Find each WBC.
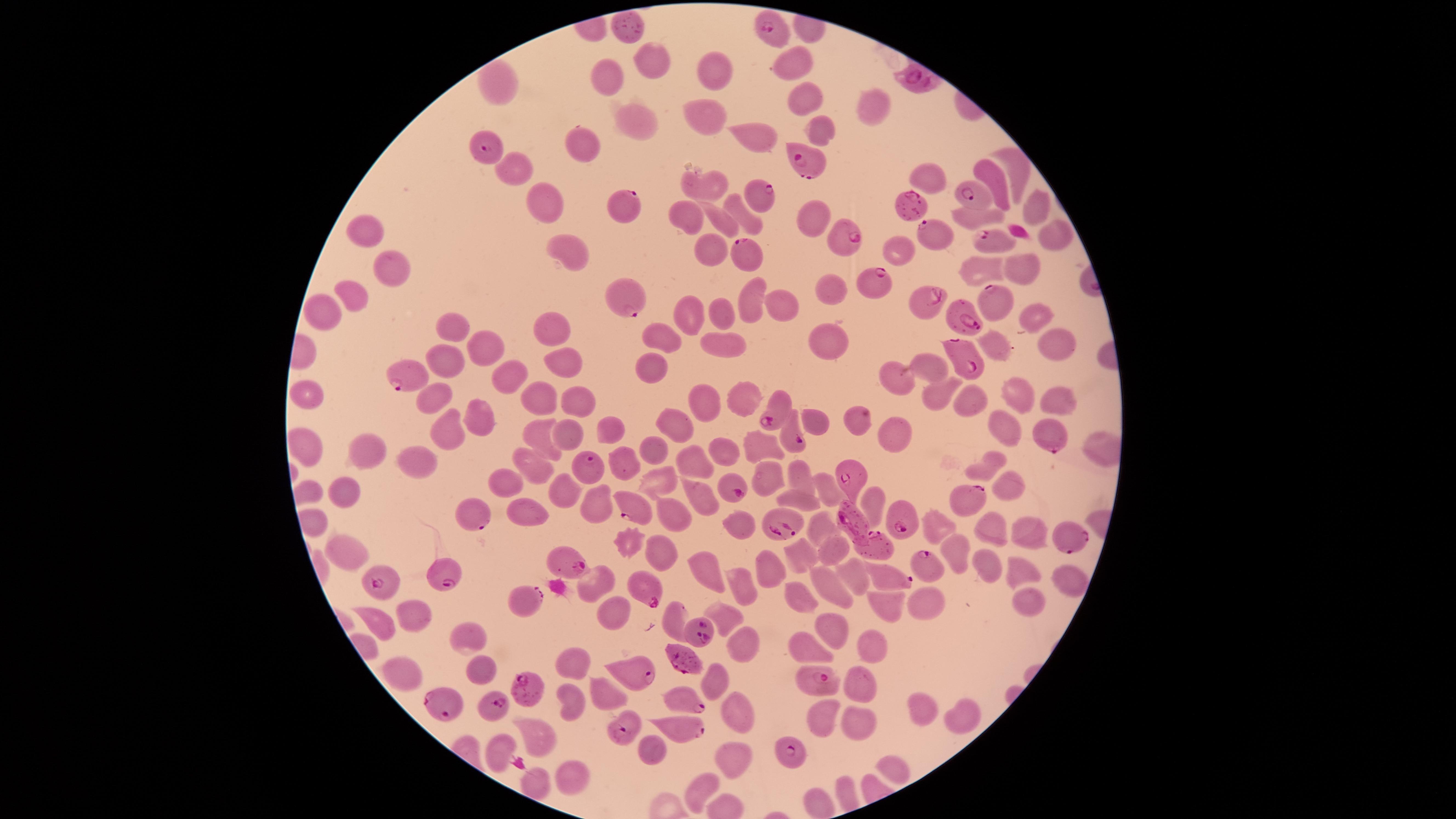
No WBCs identified.

stain = Giemsa
preparation = thin blood film
species = Plasmodium falciparum
field of view = single
uninfected RBCs = approximate marker points as (x, y) in pixels: (624, 32), (795, 59), (652, 62), (718, 70), (605, 76), (493, 80), (798, 94), (872, 110), (705, 115), (636, 122), (819, 127), (755, 133), (584, 146), (1012, 167), (511, 168), (993, 175), (929, 178), (709, 186), (542, 202), (1035, 206), (744, 214), (688, 216), (814, 218), (719, 219), (371, 230), (1050, 230), (566, 250), (709, 254), (1017, 265), (984, 267), (394, 268), (832, 288), (351, 290), (751, 296), (780, 298), (717, 315), (1035, 315), (691, 316), (331, 317), (453, 320), (552, 330), (664, 338), (1060, 342), (723, 345), (826, 346), (1001, 346), (493, 352), (444, 353), (565, 364), (935, 367), (646, 368), (511, 380), (901, 381), (1020, 390), (312, 392), (428, 395), (942, 395), (974, 395), (538, 399), (1060, 399), (705, 402), (740, 402), (581, 403), (818, 415), (481, 419), (852, 419), (678, 424), (1005, 425), (896, 426), (611, 427), (539, 433), (452, 434), (568, 434), (761, 446), (365, 449), (725, 450), (1095, 450), (654, 451), (424, 460), (625, 460), (696, 460), (530, 462), (983, 466), (796, 469), (775, 476), (662, 481), (507, 484), (559, 485), (827, 485), (1008, 486), (698, 491), (347, 493), (799, 493), (875, 499), (592, 502), (527, 510), (677, 512), (741, 523), (825, 523), (933, 523), (1029, 528), (995, 529), (630, 541), (834, 545), (960, 545), (799, 546), (344, 548), (659, 551), (989, 559), (1018, 568), (769, 569), (710, 571), (857, 575), (1067, 579), (833, 587), (744, 588), (801, 594), (1027, 598), (882, 604), (924, 605), (728, 613), (614, 614), (418, 615), (381, 618), (676, 619), (838, 626), (471, 635), (744, 638), (874, 646), (812, 650), (568, 659), (482, 667), (402, 673), (713, 682), (860, 687), (606, 694), (572, 697), (746, 711), (922, 713), (961, 717), (821, 726), (857, 729), (539, 736), (649, 746), (493, 749), (726, 758), (893, 764), (568, 776), (530, 782), (698, 788), (846, 793), (822, 798)
capture = smartphone photograph through the microscope eyepiece
visible region = circular
parasitized RBCs = approximate marker points as (x, y) in pixels: (767, 25), (919, 79), (486, 147), (807, 160), (759, 194), (974, 199), (631, 205), (916, 205), (933, 231), (846, 235), (995, 238), (743, 255), (876, 280), (628, 290), (922, 299), (995, 300), (962, 313), (964, 356), (407, 377), (770, 411), (1054, 440), (798, 443), (594, 466), (852, 476), (736, 482), (971, 501), (634, 506), (479, 516), (907, 516), (846, 519), (774, 523), (1067, 541), (873, 544), (927, 564), (574, 568), (440, 573), (381, 574), (892, 577), (651, 593), (528, 605), (698, 629), (687, 659), (639, 670), (816, 678), (523, 685), (681, 700), (443, 701), (494, 708), (621, 727), (681, 727), (785, 748)
image size = 1456×819 pixels
presence = malaria parasites seen